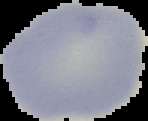

Summary:
  - Preparation: thin blood smear
  - Image type: cell region segmented out of the field of view; surrounding area masked to black
  - Malaria status: uninfected
  - Image size: 148×121 pixels